Report the malaria status of this cell.
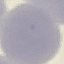

Uninfected.

{
  "stain": "Giemsa",
  "image_type": "cell patch, automatically extracted from a larger field of view and resized to 64 × 64 pixels",
  "capture": "smartphone camera at the microscope eyepiece",
  "preparation": "thin blood film"
}